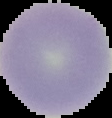 The area outside the segmented cell region is set to black. Malaria status: uninfected. Image is 112×118 pixels. From a thin blood smear.